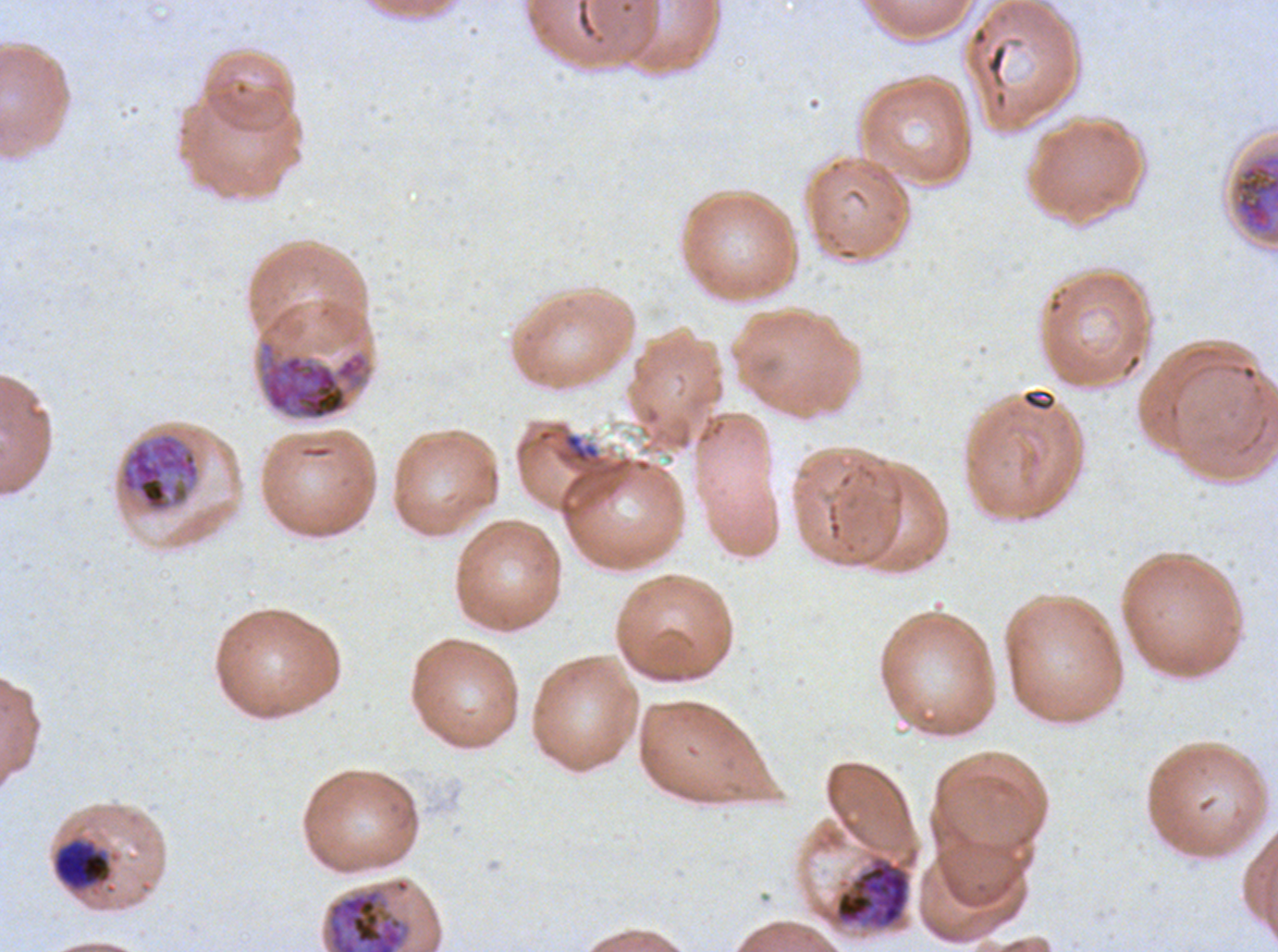

Approximate bounding boxes as {x1, y1, x2, y2} in pixels.
Summary:
  - Late schizont locations: {1233, 153, 1277, 236}, {326, 887, 411, 951}
  - Early schizont locations: {258, 339, 372, 421}, {119, 432, 201, 513}, {834, 857, 910, 928}
  - Mid trophozoite locations: {53, 839, 112, 891}
  - Debris locations: {562, 433, 600, 465}
  - Stain: Giemsa
  - Image size: 1278×952 pixels
  - Field of view: one sub-image of a larger composite
  - Preparation: thin blood film
  - Specimen: ex-vivo P. falciparum culture from a patient in The Gambia, grown for 24 to 48 hours
  - Life-cycle stages observed: mid trophozoite, early schizont, late schizont